Give the position of every Plasmodium parasite visible.
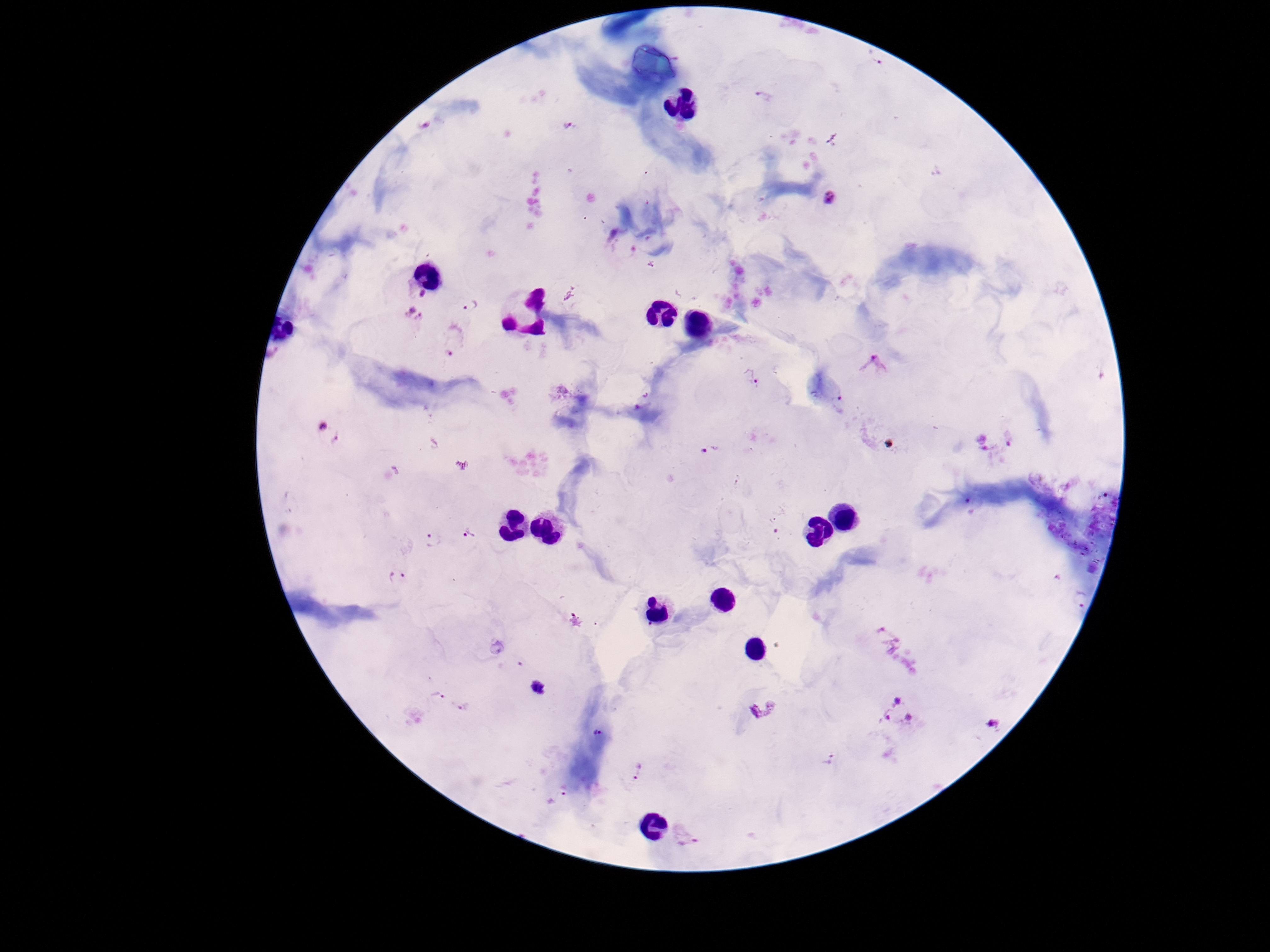

Approximate object centers, in pixels from the top-left corner.
Plasmodium parasites: (x=873, y=58), (x=764, y=97), (x=568, y=125), (x=830, y=197), (x=422, y=294), (x=470, y=305), (x=413, y=315), (x=450, y=349), (x=877, y=365), (x=751, y=376), (x=839, y=404), (x=328, y=434), (x=711, y=449), (x=471, y=534), (x=432, y=540), (x=398, y=576), (x=437, y=696), (x=466, y=706), (x=762, y=710), (x=895, y=712), (x=994, y=723), (x=597, y=732), (x=829, y=759), (x=638, y=771).

image size = 1270×952 pixels
magnification = 100x
patient malaria status = positive
preparation = thick peripheral-blood smear
stain = Giemsa
field of view = one from this slide
capture = smartphone camera through the microscope eyepiece